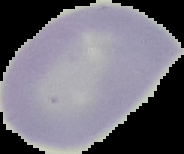

Malaria status: uninfected. Image is 184×154 pixels. From a thin blood smear. The area outside the segmented cell region is set to black.